Classify this cell by malaria status.
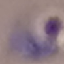
Parasitized.

image_type: cell patch, automatically extracted from a larger field of view and resized to 64 × 64 pixels
preparation: thin smear
capture: smartphone camera at the microscope eyepiece
stain: Giemsa